Give the position of every leukocyte visible.
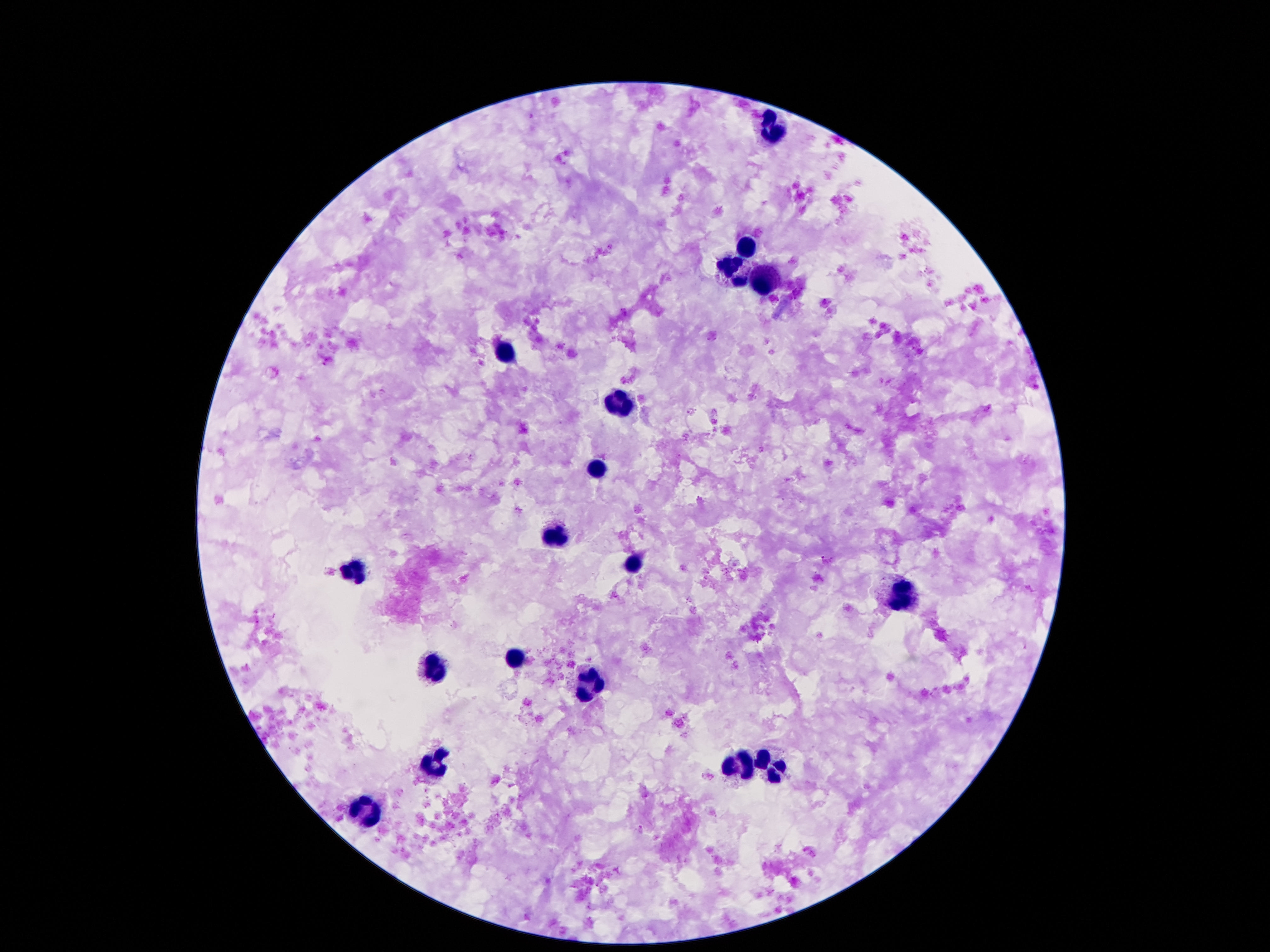
Approximate centers as {x, y} in pixels.
Leukocytes: {771, 133}, {747, 245}, {730, 269}, {763, 282}, {500, 353}, {619, 406}, {597, 469}, {560, 536}, {633, 563}, {354, 575}, {900, 592}, {517, 653}, {435, 668}, {591, 681}, {435, 760}, {737, 765}, {771, 765}, {365, 813}.

Summary:
  - Capture: smartphone camera through the microscope eyepiece
  - Patient malaria status: uninfected
  - Stain: Giemsa
  - Image size: 1270×952 pixels
  - Magnification: 100x
  - Preparation: thick blood film
  - Field of view: single